Point out each Plasmodium parasite.
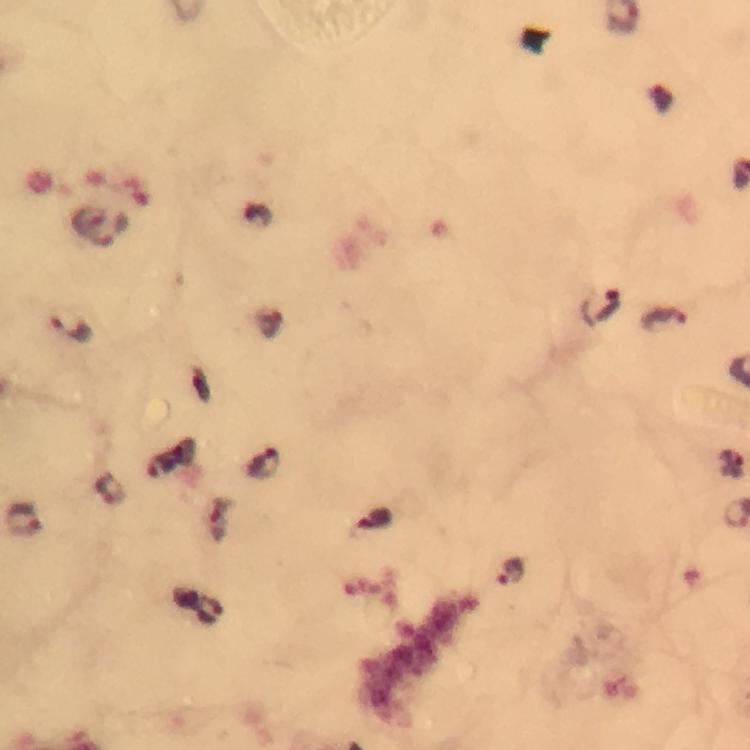

Approximate centers as {x, y} in pixels.
Plasmodium parasites: {88, 218}, {599, 307}, {664, 320}, {70, 328}, {265, 464}, {108, 490}, {23, 519}, {218, 520}, {373, 520}, {512, 572}, {209, 612}.

Summary:
  - Image size: 750×750 pixels
  - Capture: smartphone photograph through a microscope
  - Magnification: 100x
  - Stain: Giemsa
  - Preparation: thick smear
  - Context: from a malaria diagnostic workup
  - Cropped from: a single field of view
  - Immersion oil: used